Comment on the morphology of the red blood cells.
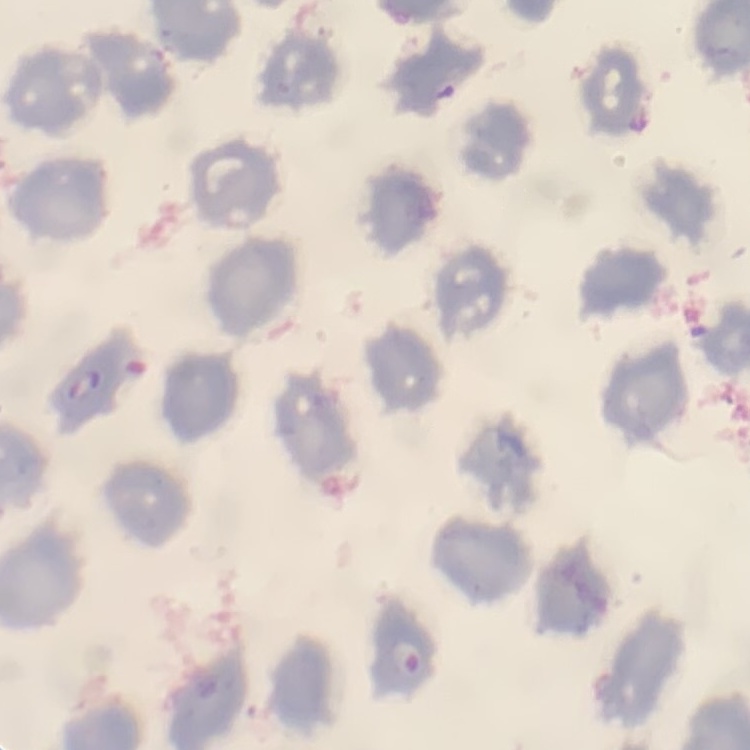

No rouleaux formation.

stain: Field's or Giemsa
image_type: square crop of a larger photomicrograph
preparation: thin peripheral smear